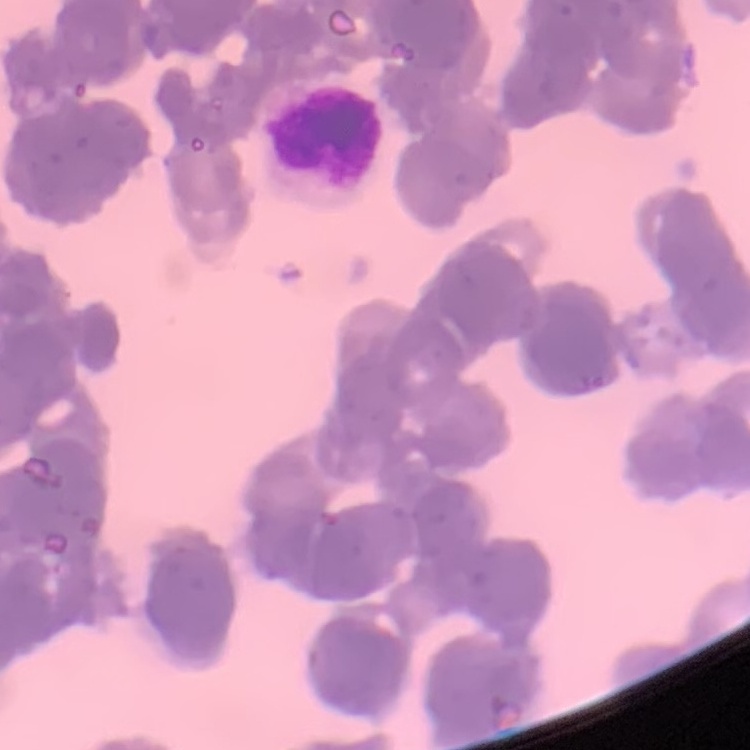

The red blood cells exhibit rouleaux formation. Square crop of a larger photomicrograph. Stained with either Field's or Giemsa. Thin blood film.